Assess the morphology of the erythrocytes.
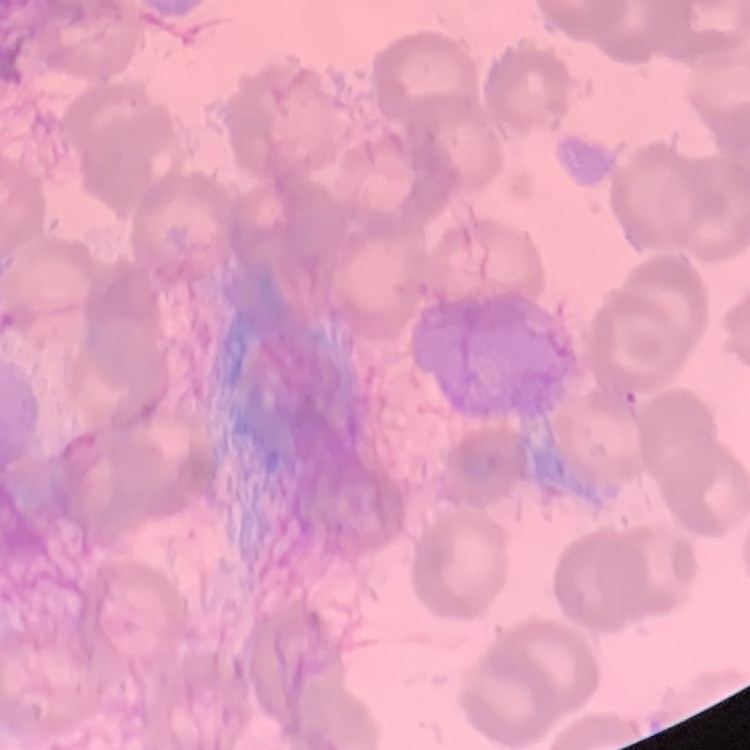
No rouleaux formation.

Summary:
  - Stain: Field's or Giemsa
  - Image type: one tile cut from a larger photomicrograph
  - Preparation: thin blood film